Locate malaria parasites and leukocytes.
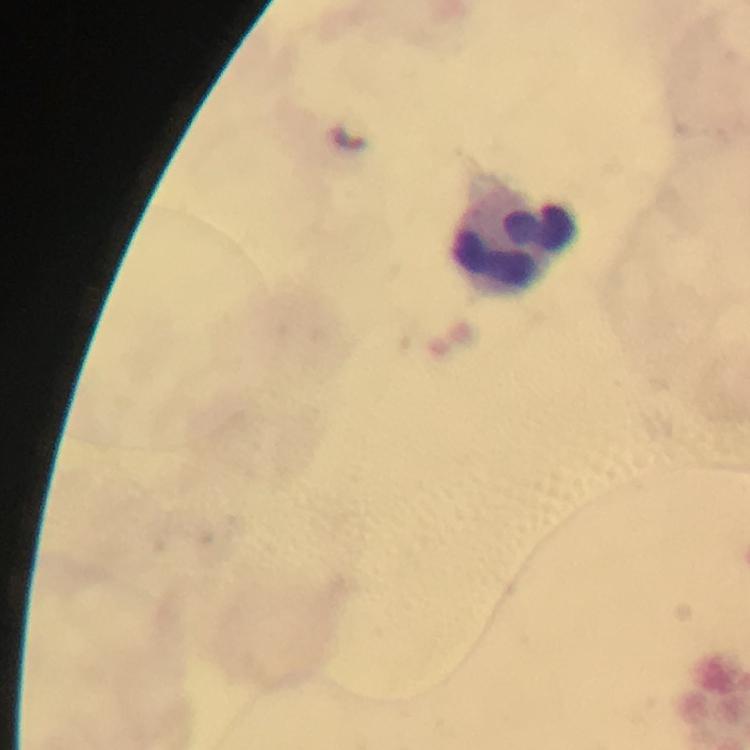

No malaria parasites detected.
Approximate object centers, in pixels from the top-left corner.
Leukocytes: (x=517, y=237).

Summary:
  - Cropped from: a single field of view
  - Stain: Giemsa
  - Capture: smartphone camera through the microscope
  - Preparation: thick smear
  - Magnification: 100x
  - Immersion oil: applied
  - Image size: 750×750 pixels
  - Context: from a malaria diagnostic workup